Assess for Plasmodium parasites.
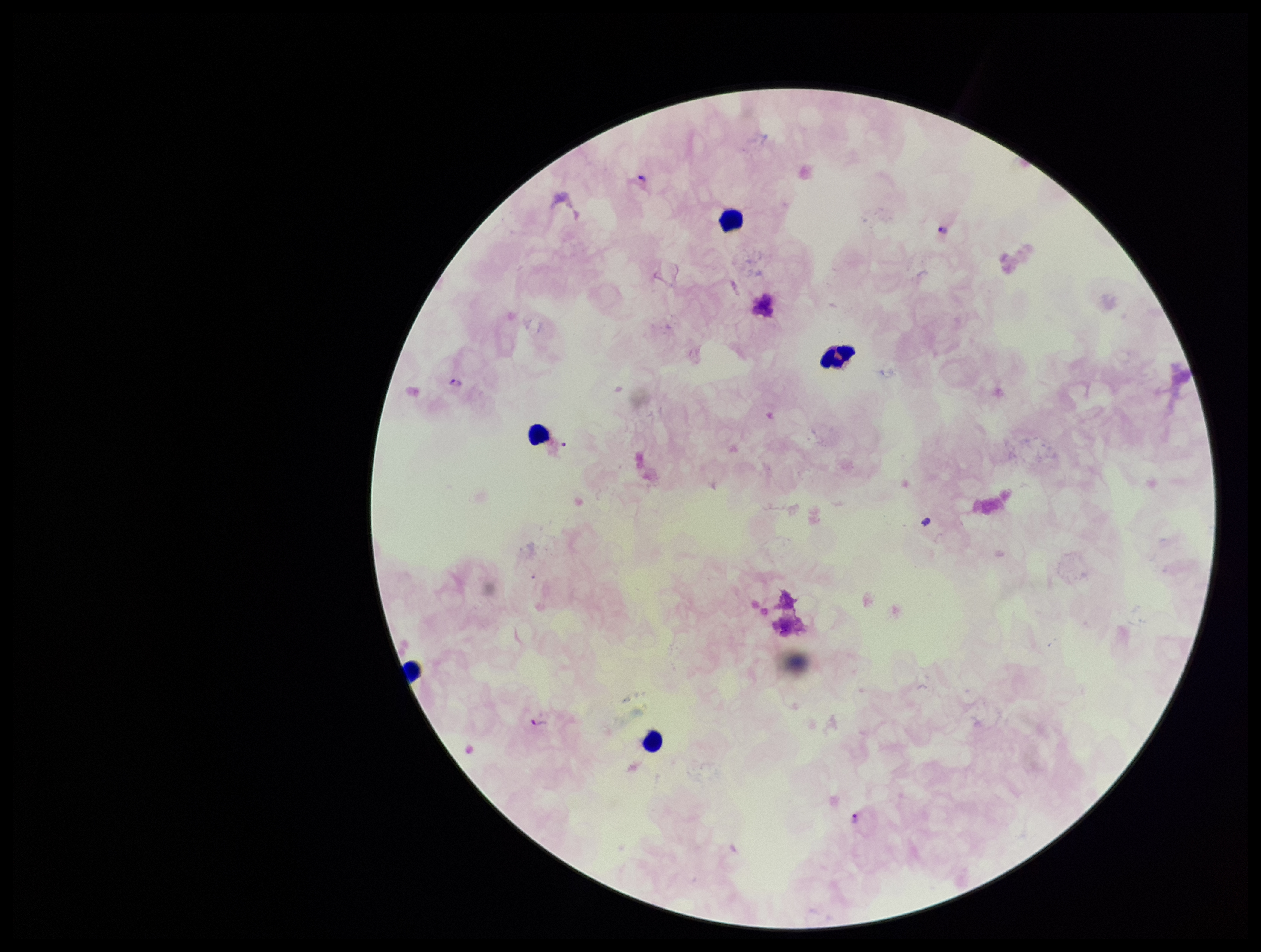

Identified.

preparation: thick blood smear
leukocyte_count: 5
image_size: 1261×952 pixels
patient_malaria_status: positive
field_of_view: single
species_reported_for_this_patient: Plasmodium falciparum
parasite_count: 4
capture: smartphone photograph through the microscope eyepiece
stain: Giemsa